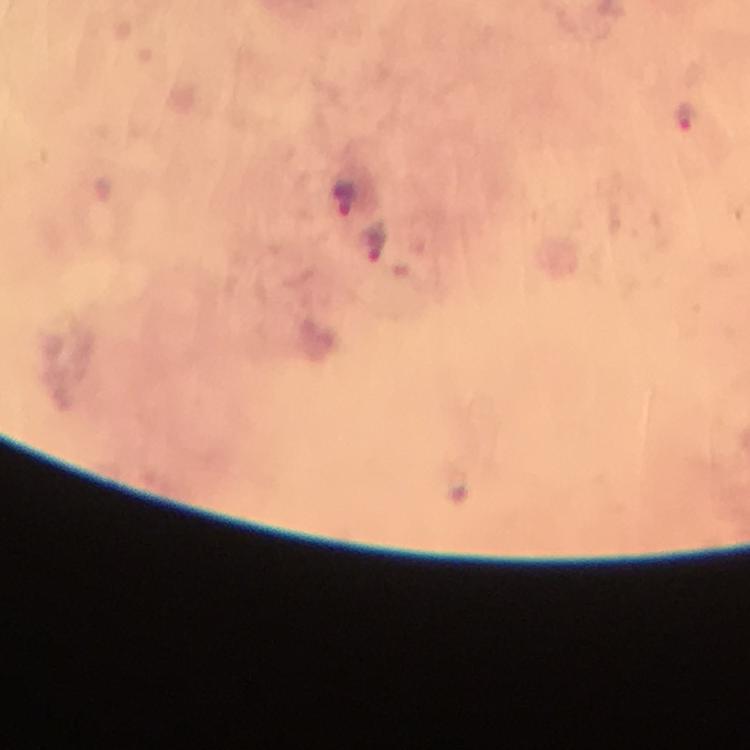
Approximate centers as (x, y) in pixels. Malaria parasite locations: (685, 117), (374, 239). Immersion oil was used. 100x magnification. Thick blood film. From a diagnostic examination for malaria. Cropped region of a single field of view. Image is 750×750 pixels. Giemsa stain. Photographed through the microscope with a smartphone camera.